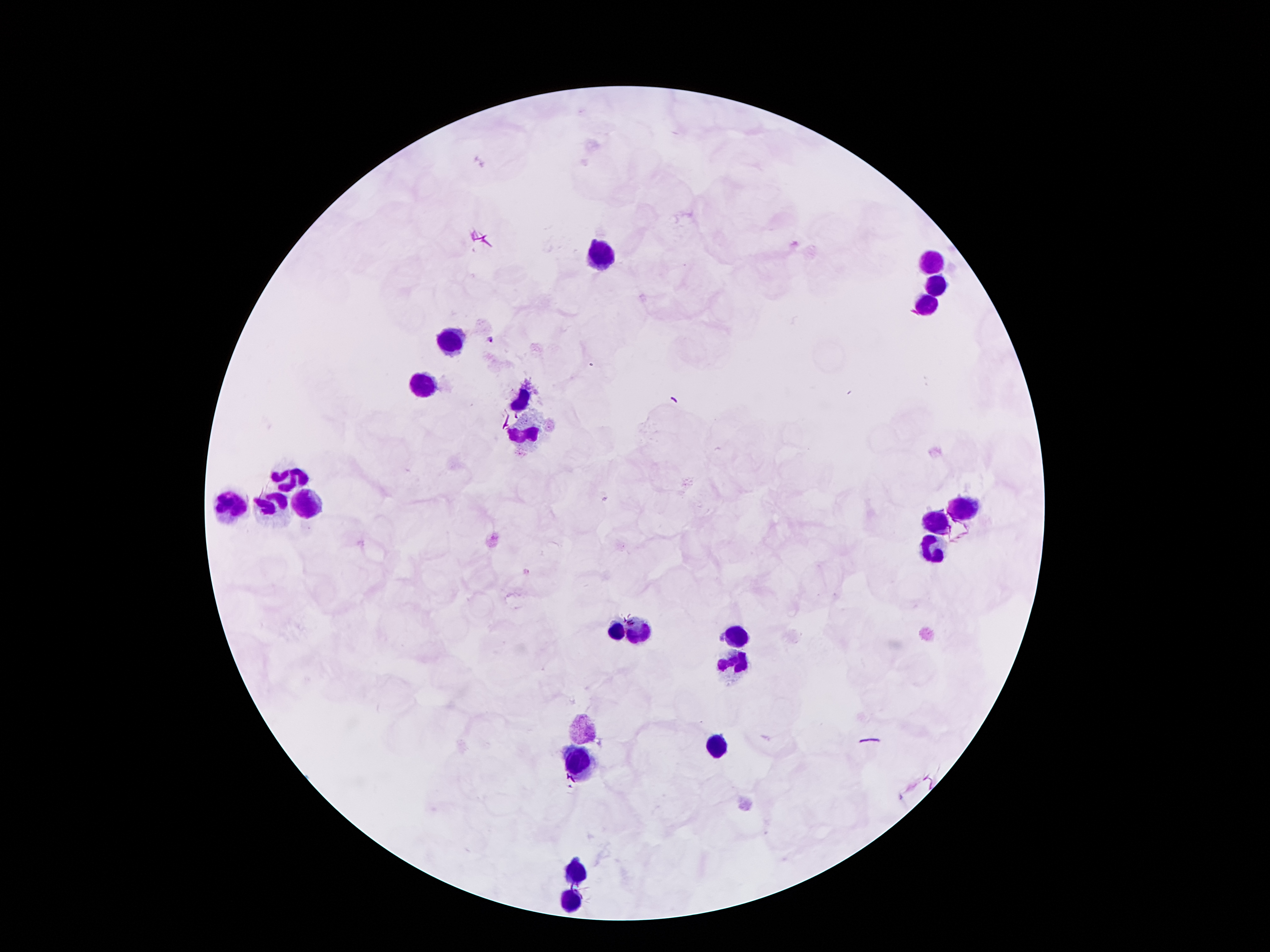 Approximate object centers, in pixels from the top-left corner. Leukocyte locations: (x=598, y=256), (x=933, y=260), (x=935, y=283), (x=927, y=302), (x=449, y=339), (x=421, y=382), (x=520, y=403), (x=526, y=436), (x=293, y=474), (x=230, y=505), (x=270, y=505), (x=308, y=505), (x=963, y=508), (x=936, y=522), (x=931, y=550), (x=616, y=629), (x=639, y=629), (x=734, y=640), (x=736, y=663), (x=583, y=730), (x=715, y=747), (x=576, y=764), (x=574, y=873), (x=572, y=900). Plasmodium parasite locations: (x=491, y=340). Image is 1270×952 pixels. Giemsa stain. 100x magnification. Patient malaria status: infected with Plasmodium falciparum. Thick blood smear. Smartphone photograph taken through the microscope eyepiece. One field from this slide.